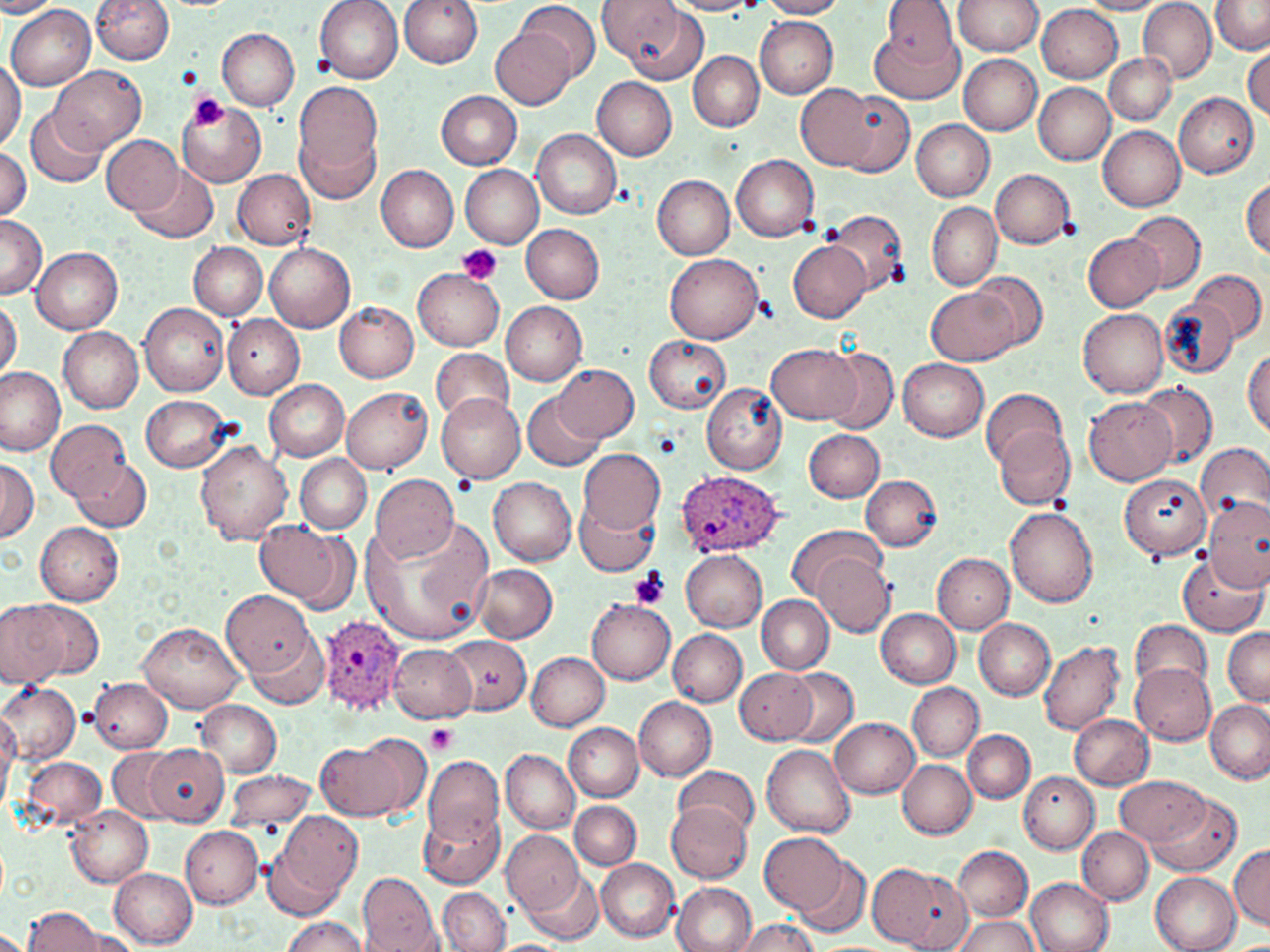

Approximate bounding boxes as (x1, y1, x2, y2) in pixels. Plasmodium ovale-infected red blood cell locations: (674, 470, 783, 557), (320, 615, 406, 714). Platelet locations: (187, 91, 229, 132), (456, 243, 502, 285), (455, 475, 477, 494), (629, 568, 670, 610), (425, 725, 457, 754). Uninfected red blood cell locations: (91, 0, 173, 65), (314, 0, 403, 83), (400, 0, 482, 69), (517, 0, 602, 83), (597, 0, 699, 76), (668, 0, 766, 16), (757, 0, 849, 18), (878, 0, 959, 73), (953, 0, 1043, 55), (1210, 0, 1269, 53), (1076, 1, 1170, 15), (1139, 1, 1216, 82), (0, 2, 60, 18), (7, 3, 96, 90), (1037, 5, 1123, 83), (755, 16, 838, 98), (869, 21, 966, 106), (491, 27, 575, 110), (217, 28, 301, 111), (1243, 46, 1270, 121), (689, 51, 764, 131), (1105, 51, 1177, 126), (959, 55, 1041, 135), (0, 57, 25, 153), (51, 65, 145, 151), (592, 77, 678, 160), (292, 80, 384, 188), (796, 83, 898, 173), (1034, 83, 1114, 165), (436, 91, 523, 169), (1174, 92, 1259, 178), (840, 93, 914, 176), (177, 100, 267, 187), (26, 107, 108, 189), (912, 120, 995, 201), (1097, 125, 1186, 210), (298, 126, 378, 207), (532, 129, 622, 218), (102, 133, 183, 214), (0, 148, 31, 219), (731, 153, 820, 242), (130, 164, 219, 244), (651, 164, 819, 251), (376, 165, 459, 252), (461, 166, 543, 247), (233, 169, 315, 250), (990, 169, 1074, 249), (653, 175, 735, 259), (1242, 176, 1270, 259), (927, 201, 1001, 290), (824, 210, 909, 297), (1125, 210, 1207, 292), (1, 215, 47, 302), (521, 223, 604, 304), (1083, 232, 1165, 312), (789, 240, 871, 323), (189, 242, 267, 320), (265, 243, 356, 332), (30, 244, 123, 334), (665, 253, 764, 342), (412, 267, 504, 352), (1190, 269, 1266, 346), (973, 271, 1048, 352), (927, 288, 1018, 367), (0, 298, 22, 380), (1159, 299, 1238, 379), (334, 301, 419, 382), (501, 301, 588, 385), (140, 302, 229, 397), (1077, 308, 1168, 397), (224, 316, 304, 398), (59, 327, 144, 413), (644, 333, 731, 414), (767, 344, 862, 424), (429, 348, 516, 423), (822, 348, 899, 435), (1244, 348, 1269, 435), (899, 359, 989, 441), (555, 363, 638, 443), (0, 365, 65, 453), (265, 379, 349, 461), (1136, 381, 1217, 469), (702, 384, 786, 474), (340, 387, 432, 474), (980, 387, 1067, 470), (524, 392, 605, 470), (436, 393, 526, 482), (140, 394, 233, 471), (1084, 396, 1177, 486), (47, 419, 130, 501), (992, 426, 1074, 509), (805, 429, 885, 502), (195, 440, 293, 545), (1197, 442, 1270, 529), (579, 449, 665, 534), (296, 455, 371, 534), (0, 456, 38, 543), (71, 457, 150, 531), (371, 472, 460, 564), (1118, 472, 1210, 558), (861, 474, 940, 551), (488, 475, 577, 565), (1203, 495, 1270, 591), (577, 501, 657, 576), (1004, 507, 1099, 607), (362, 519, 489, 644), (254, 520, 357, 608), (35, 523, 124, 605), (786, 524, 882, 602), (681, 550, 767, 631), (1177, 551, 1268, 638), (932, 553, 1014, 632), (814, 555, 895, 635), (474, 563, 557, 642), (223, 592, 315, 678), (757, 595, 834, 675), (0, 599, 66, 687), (588, 599, 675, 683), (21, 601, 105, 680), (877, 608, 961, 687), (972, 618, 1055, 699), (1131, 619, 1212, 694), (137, 623, 244, 712), (1222, 626, 1270, 706), (669, 628, 746, 705), (245, 630, 332, 710), (445, 635, 534, 715), (1037, 640, 1124, 736), (389, 644, 476, 723), (526, 652, 610, 729), (1130, 662, 1216, 743), (733, 667, 820, 744), (781, 667, 859, 748), (89, 677, 172, 753), (0, 682, 81, 763), (907, 683, 984, 762), (633, 696, 716, 780), (1204, 698, 1270, 784), (196, 700, 281, 777), (1070, 714, 1155, 791), (0, 717, 19, 793), (830, 717, 920, 798), (565, 723, 644, 801), (963, 730, 1034, 802), (317, 736, 422, 821), (146, 743, 229, 825), (761, 744, 856, 838), (108, 749, 182, 823), (500, 749, 580, 833), (19, 757, 104, 827), (425, 757, 504, 844), (899, 759, 976, 839), (675, 765, 758, 835), (224, 770, 316, 829), (1020, 772, 1098, 854), (1117, 774, 1208, 846), (1149, 793, 1242, 876), (666, 800, 752, 883), (570, 801, 641, 869), (64, 803, 152, 886), (421, 809, 503, 887), (268, 812, 365, 912), (180, 826, 265, 908), (1077, 826, 1154, 905), (501, 830, 585, 913), (759, 831, 851, 916), (954, 845, 1033, 921), (1230, 845, 1270, 929), (790, 854, 871, 939), (596, 858, 679, 941), (876, 866, 973, 952), (109, 868, 198, 948), (359, 871, 445, 950), (522, 872, 600, 944), (1151, 872, 1241, 952), (1026, 878, 1114, 952), (673, 881, 756, 952), (439, 887, 509, 951), (22, 908, 106, 951), (279, 916, 370, 952), (952, 916, 1040, 952), (734, 918, 819, 952), (0, 927, 28, 952), (64, 928, 146, 951). Slide-level diagnosis: Plasmodium ovale. Single field of view. Image is 1270×952 pixels. Captured at 1000x magnification. Optical microscopy. Thin blood film. May-Grünwald-Giemsa stain.